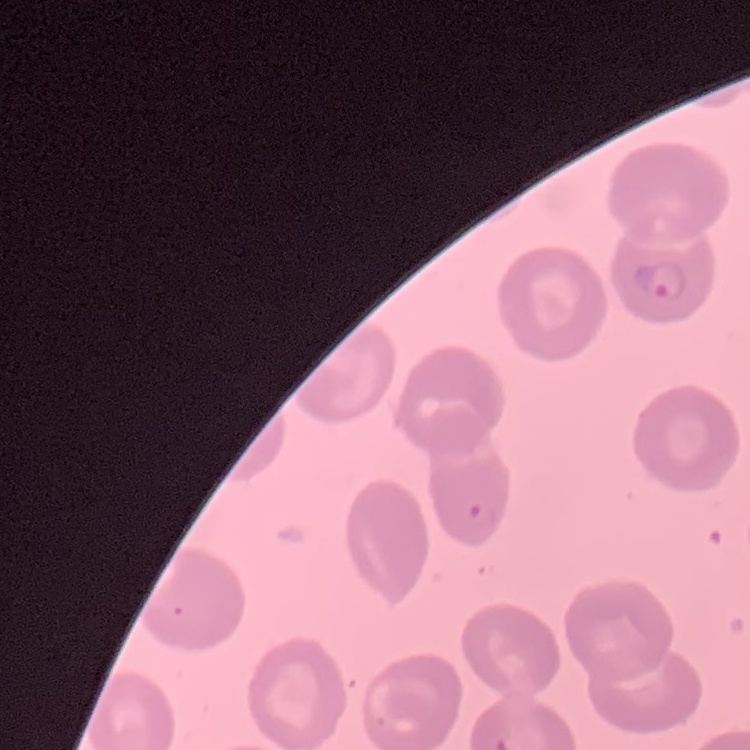
The erythrocytes exhibit no rouleaux formation. Thin blood smear. Stained with either Field's or Giemsa. One tile cut from a larger photomicrograph.